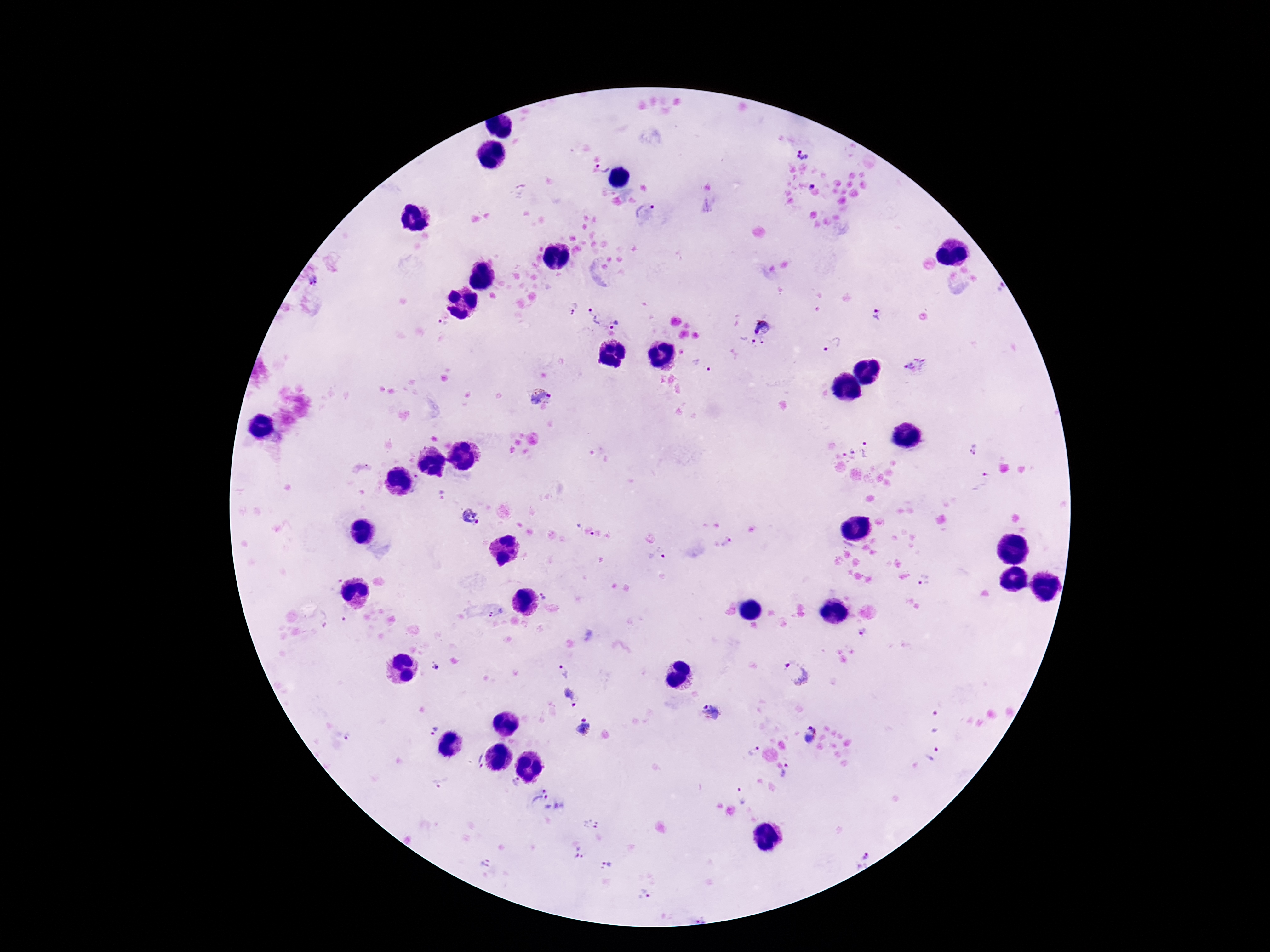
Approximate centers as (x, y) in pixels.
Summary:
  - Plasmodium parasite locations: (802, 152), (605, 164), (813, 184), (646, 211), (313, 281), (1001, 286), (572, 309), (876, 313), (593, 317), (763, 324), (617, 325), (442, 326), (758, 343), (833, 344), (916, 365), (702, 366), (540, 398), (973, 448), (868, 450), (848, 454), (980, 482), (440, 495), (470, 517), (723, 541), (658, 555), (924, 580), (333, 584), (543, 592), (496, 612), (862, 632), (433, 665), (563, 672), (795, 673), (570, 695), (711, 711), (935, 722), (583, 727), (434, 731), (810, 733), (350, 738), (752, 751), (931, 754), (477, 762), (788, 770), (516, 781), (441, 783), (743, 795), (551, 801), (592, 825), (579, 854), (863, 860), (485, 862), (608, 863), (645, 894)
  - Magnification: 100x
  - Preparation: thick peripheral-blood smear
  - Patient malaria status: positive
  - Capture: smartphone camera through the microscope eyepiece
  - Image size: 1270×952 pixels
  - Stain: Giemsa
  - Field of view: single